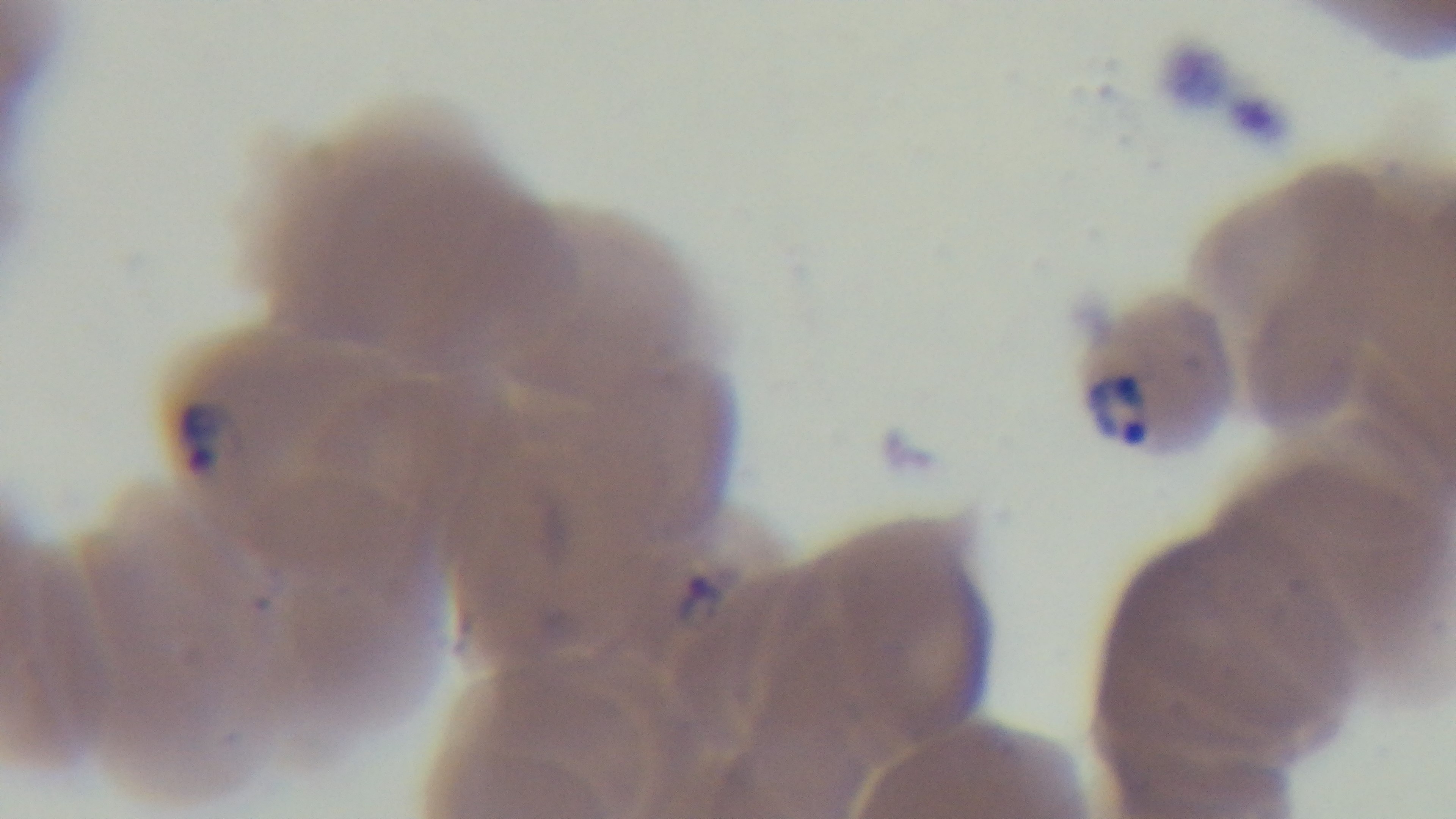
Single field of view. Light microscopy. Preparation: thin. 100x oil-immersion objective. Giemsa-stained. Mounted 4K digital camera. Malaria status: infected.